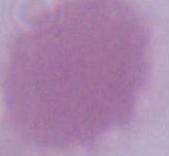
{
  "modality": "photomicrograph",
  "identification": "red blood cell",
  "magnification": "1000x"
}